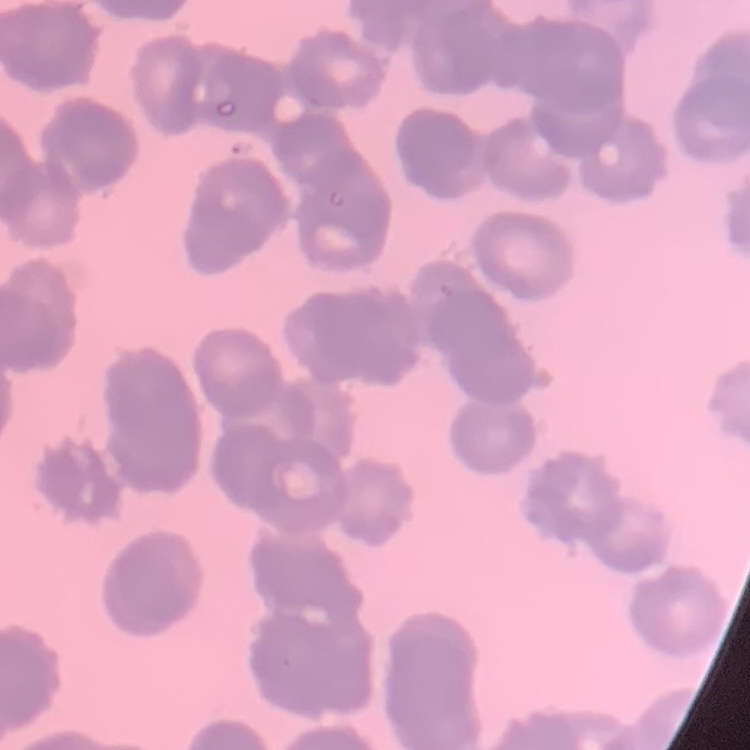
erythrocyte morphology = rouleaux formation
preparation = thin blood film
stain = Field's or Giemsa
image type = square crop of a larger photomicrograph